Outline each blood parasite and name the species.
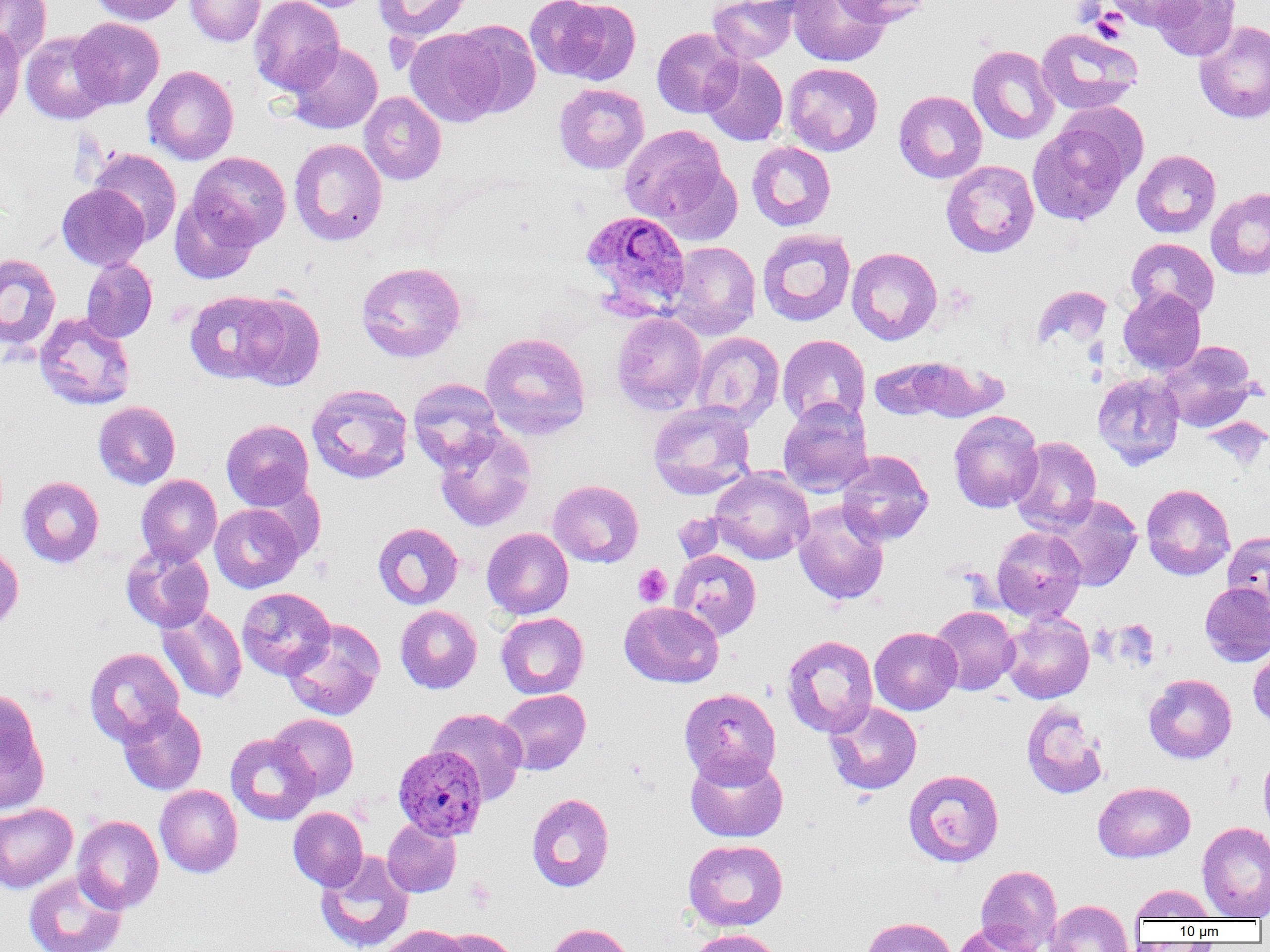

Approximate bounding boxes as named x1/y1/x2/y2 corners in pixels.
Plasmodium ovale-infected red blood cells: (x1=581, y1=210, x2=691, y2=315), (x1=393, y1=744, x2=487, y2=839).
No Plasmodium falciparum, Plasmodium malariae, Plasmodium vivax, Babesia divergens, or Trypanosoma brucei observed.

Summary:
  - Platelet locations: (x1=1072, y1=1, x2=1106, y2=25), (x1=1092, y1=10, x2=1128, y2=44), (x1=633, y1=564, x2=672, y2=606)
  - Uninfected red blood cell locations: (x1=0, y1=0, x2=51, y2=64), (x1=89, y1=0, x2=188, y2=25), (x1=185, y1=0, x2=265, y2=46), (x1=249, y1=0, x2=344, y2=95), (x1=280, y1=0, x2=377, y2=12), (x1=374, y1=0, x2=472, y2=41), (x1=525, y1=0, x2=625, y2=82), (x1=707, y1=0, x2=798, y2=63), (x1=788, y1=0, x2=891, y2=67), (x1=835, y1=0, x2=933, y2=27), (x1=1105, y1=0, x2=1201, y2=30), (x1=1150, y1=0, x2=1240, y2=61), (x1=70, y1=18, x2=164, y2=109), (x1=1194, y1=19, x2=1270, y2=123), (x1=448, y1=20, x2=541, y2=119), (x1=0, y1=26, x2=25, y2=128), (x1=651, y1=27, x2=743, y2=118), (x1=1036, y1=27, x2=1143, y2=115), (x1=404, y1=28, x2=505, y2=127), (x1=21, y1=31, x2=114, y2=125), (x1=286, y1=42, x2=383, y2=134), (x1=968, y1=45, x2=1059, y2=144), (x1=700, y1=54, x2=788, y2=146), (x1=783, y1=62, x2=883, y2=156), (x1=143, y1=65, x2=238, y2=165), (x1=554, y1=83, x2=649, y2=174), (x1=894, y1=90, x2=987, y2=183), (x1=359, y1=92, x2=446, y2=185), (x1=1028, y1=118, x2=1134, y2=227), (x1=619, y1=124, x2=731, y2=228), (x1=289, y1=138, x2=388, y2=245), (x1=746, y1=141, x2=836, y2=231), (x1=88, y1=148, x2=182, y2=246), (x1=1132, y1=149, x2=1220, y2=238), (x1=188, y1=151, x2=291, y2=249), (x1=941, y1=160, x2=1040, y2=258), (x1=57, y1=184, x2=150, y2=270), (x1=1206, y1=188, x2=1270, y2=279), (x1=170, y1=195, x2=259, y2=283), (x1=757, y1=228, x2=856, y2=326), (x1=1126, y1=238, x2=1219, y2=318), (x1=665, y1=241, x2=760, y2=340), (x1=846, y1=247, x2=943, y2=345), (x1=0, y1=253, x2=61, y2=350), (x1=81, y1=258, x2=158, y2=343), (x1=356, y1=261, x2=466, y2=363), (x1=1031, y1=285, x2=1112, y2=351), (x1=1118, y1=288, x2=1206, y2=375), (x1=185, y1=291, x2=286, y2=383), (x1=235, y1=294, x2=326, y2=390), (x1=34, y1=312, x2=136, y2=410), (x1=611, y1=312, x2=708, y2=414), (x1=480, y1=332, x2=591, y2=440), (x1=690, y1=332, x2=784, y2=428), (x1=778, y1=335, x2=870, y2=427), (x1=1159, y1=341, x2=1258, y2=432), (x1=905, y1=357, x2=1006, y2=422), (x1=869, y1=359, x2=953, y2=421), (x1=1093, y1=373, x2=1184, y2=469), (x1=407, y1=378, x2=504, y2=471), (x1=306, y1=383, x2=413, y2=484), (x1=778, y1=397, x2=873, y2=497), (x1=93, y1=401, x2=180, y2=489), (x1=648, y1=401, x2=756, y2=500), (x1=949, y1=410, x2=1044, y2=513), (x1=1203, y1=417, x2=1268, y2=471), (x1=221, y1=419, x2=314, y2=510), (x1=434, y1=425, x2=537, y2=532), (x1=1010, y1=436, x2=1102, y2=535), (x1=836, y1=450, x2=933, y2=545), (x1=709, y1=468, x2=814, y2=564), (x1=136, y1=475, x2=222, y2=565), (x1=18, y1=476, x2=104, y2=567), (x1=548, y1=480, x2=643, y2=567), (x1=1141, y1=484, x2=1235, y2=580), (x1=1046, y1=494, x2=1143, y2=592), (x1=793, y1=501, x2=889, y2=606), (x1=210, y1=503, x2=304, y2=593), (x1=671, y1=513, x2=728, y2=565), (x1=373, y1=522, x2=463, y2=610), (x1=383, y1=522, x2=470, y2=694), (x1=991, y1=526, x2=1086, y2=622), (x1=482, y1=527, x2=573, y2=619), (x1=1222, y1=531, x2=1269, y2=611), (x1=0, y1=544, x2=23, y2=635), (x1=121, y1=546, x2=214, y2=632), (x1=669, y1=549, x2=761, y2=641), (x1=1200, y1=581, x2=1270, y2=666), (x1=237, y1=587, x2=335, y2=680), (x1=619, y1=601, x2=724, y2=688), (x1=157, y1=604, x2=247, y2=704), (x1=395, y1=605, x2=482, y2=694), (x1=929, y1=605, x2=1019, y2=695), (x1=496, y1=612, x2=589, y2=699), (x1=1000, y1=612, x2=1094, y2=704), (x1=282, y1=619, x2=385, y2=720), (x1=869, y1=627, x2=962, y2=715), (x1=781, y1=635, x2=878, y2=737), (x1=84, y1=647, x2=184, y2=746), (x1=1248, y1=647, x2=1270, y2=729), (x1=1144, y1=674, x2=1236, y2=763), (x1=679, y1=688, x2=781, y2=785), (x1=0, y1=689, x2=48, y2=812), (x1=495, y1=689, x2=591, y2=775), (x1=823, y1=701, x2=922, y2=795), (x1=1020, y1=702, x2=1108, y2=799), (x1=118, y1=703, x2=206, y2=794), (x1=427, y1=708, x2=528, y2=804), (x1=269, y1=713, x2=359, y2=800), (x1=225, y1=733, x2=320, y2=825), (x1=685, y1=750, x2=788, y2=843), (x1=1258, y1=750, x2=1270, y2=840), (x1=903, y1=769, x2=1004, y2=867), (x1=1093, y1=781, x2=1195, y2=863), (x1=154, y1=785, x2=242, y2=877), (x1=526, y1=793, x2=615, y2=892), (x1=0, y1=803, x2=78, y2=893), (x1=288, y1=807, x2=368, y2=891), (x1=72, y1=815, x2=164, y2=913), (x1=382, y1=819, x2=461, y2=897), (x1=1197, y1=821, x2=1270, y2=920), (x1=682, y1=839, x2=789, y2=932), (x1=314, y1=851, x2=414, y2=952), (x1=976, y1=865, x2=1062, y2=952), (x1=24, y1=869, x2=127, y2=952), (x1=1129, y1=884, x2=1218, y2=922), (x1=1045, y1=900, x2=1134, y2=952), (x1=861, y1=917, x2=957, y2=952), (x1=545, y1=923, x2=637, y2=952), (x1=953, y1=923, x2=1043, y2=952), (x1=380, y1=925, x2=470, y2=952), (x1=438, y1=928, x2=520, y2=952), (x1=687, y1=928, x2=784, y2=952)
  - Slide-level diagnosis: Plasmodium ovale
  - Image size: 1270×952 pixels
  - Field of view: one of a larger specimen
  - Magnification: 1000x
  - Modality: light microscopy
  - Preparation: thin blood film